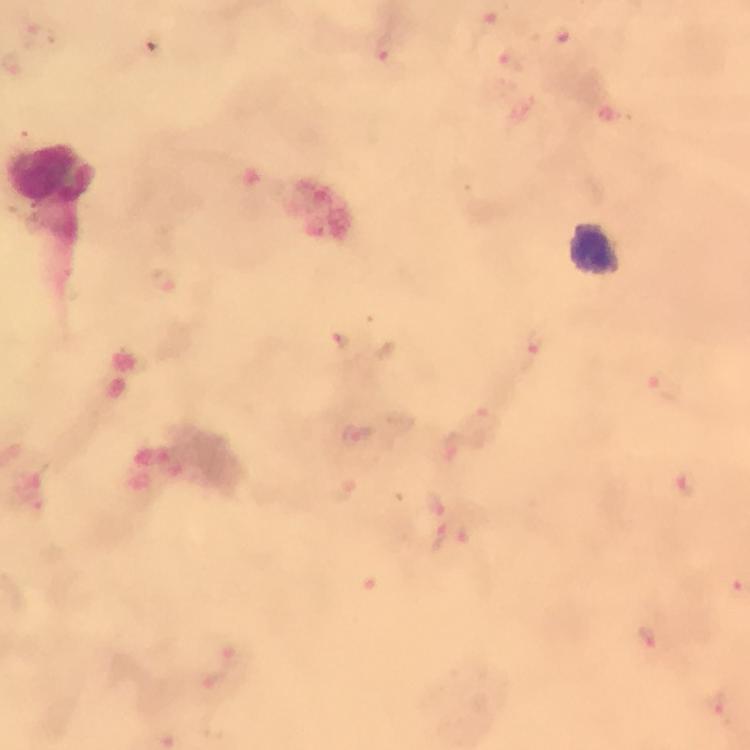
stain: Giemsa
magnification: 100x
malaria_parasite_locations: 'approximate centers as {x, y} in pixels: {492, 23}, {567, 43}, {386, 50}, {512, 59}, {161, 280}, {344, 340}, {531, 343}, {664, 385}, {479, 420}, {359, 436}, {687, 484}, {435, 502}, {439, 536}, {648, 636}, {230, 651}, {716, 704}'
leukocyte_locations: 'approximate centers as {x, y} in pixels: {51, 176}, {592, 247}'
preparation: thick blood film
image_size: 750×750 pixels
immersion_oil: used
cropped_from: one field of view
capture: smartphone camera through the microscope
context: from a malaria diagnostic workup